Report the malaria status of this cell.
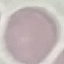

It is uninfected.

Summary:
  - Preparation: thin blood film
  - Stain: Giemsa
  - Image type: cell patch, automatically extracted from a larger field of view and resized to 64 × 64 pixels
  - Capture: smartphone camera at the microscope eyepiece